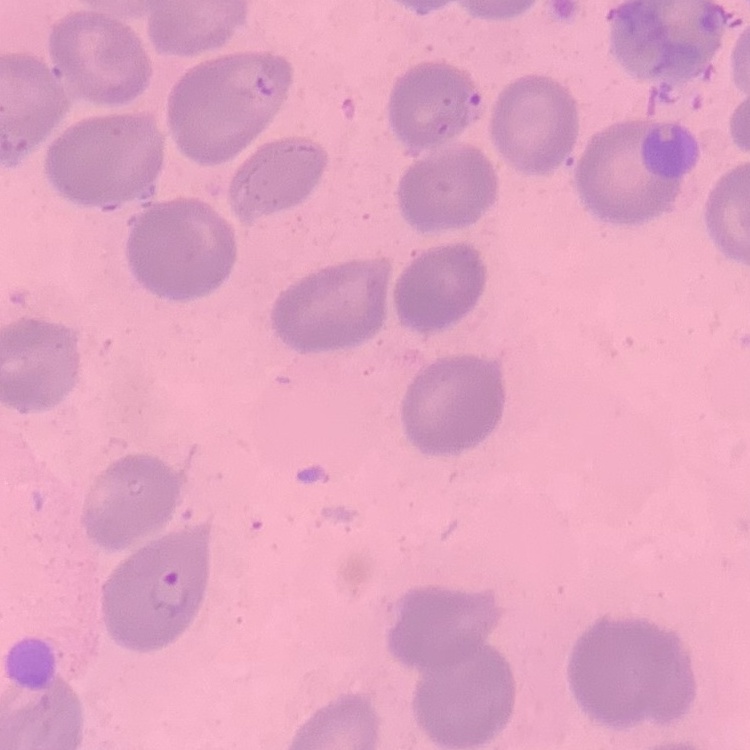
The erythrocytes exhibit no rouleaux formation. Field's or Giemsa stain. One tile cut from a larger photomicrograph. Thin blood smear.